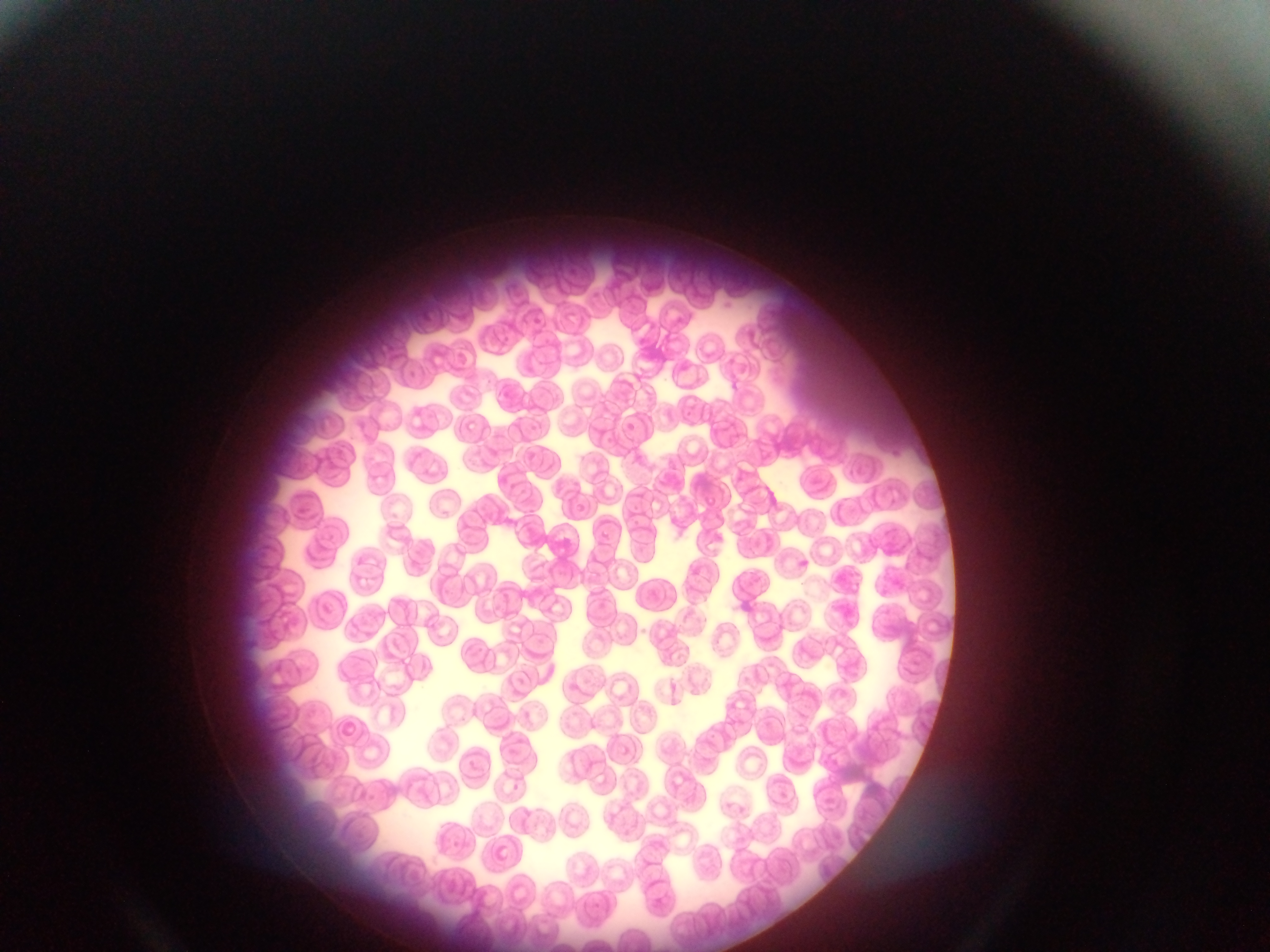
Approximate bounding boxes as [left, top, right, bottom] in pixels. Malaria parasite locations: [528, 315, 544, 326], [621, 421, 638, 438], [595, 528, 614, 546], [512, 783, 523, 795] | approximate [x, y] pixel centers of objects too small to bound: [472, 762], [786, 793]. Mobile-phone photograph taken through the microscope. Collected in Ghana. Single field of view. Thin blood film. Image is 1270×952 pixels.